Give a bounding box for every leukocyte visible.
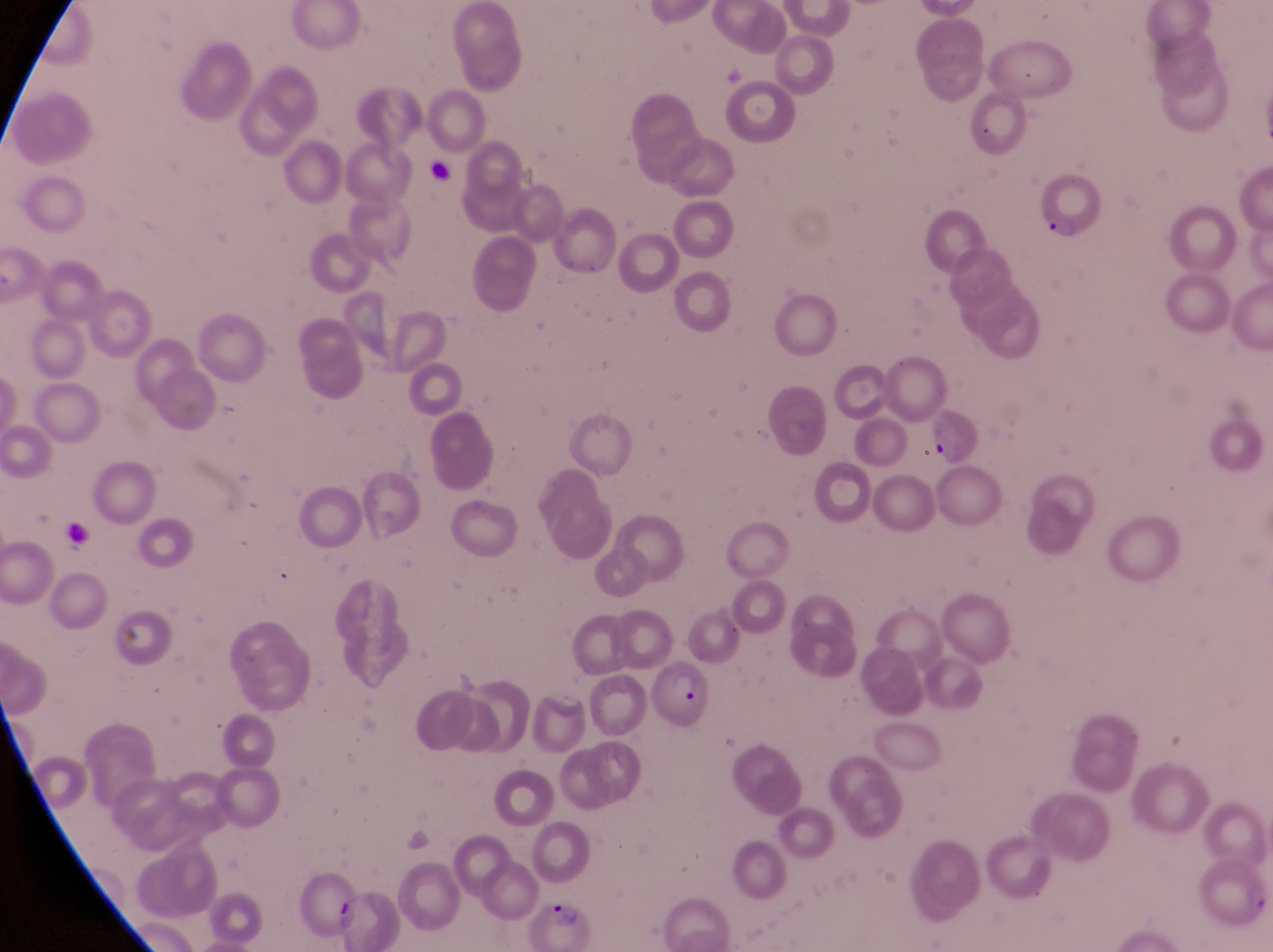
No leukocytes observed.

Approximate bounding boxes as {left, top, right, bottom} in pixels. Artifact (platelet-like body, stain precipitate, or debris) locations: {429, 160, 454, 188}, {58, 515, 98, 550}. Parasitised red blood cell locations: {1034, 169, 1103, 251}, {924, 399, 989, 474}, {641, 656, 715, 726}, {529, 891, 598, 952}. Image is 1273×952 pixels. Thin blood film. Single field of view. Collected in Uganda. Photographed through the eyepiece of an Olympus CX-23 microscope with a smartphone camera. At a magnification of 1000x.